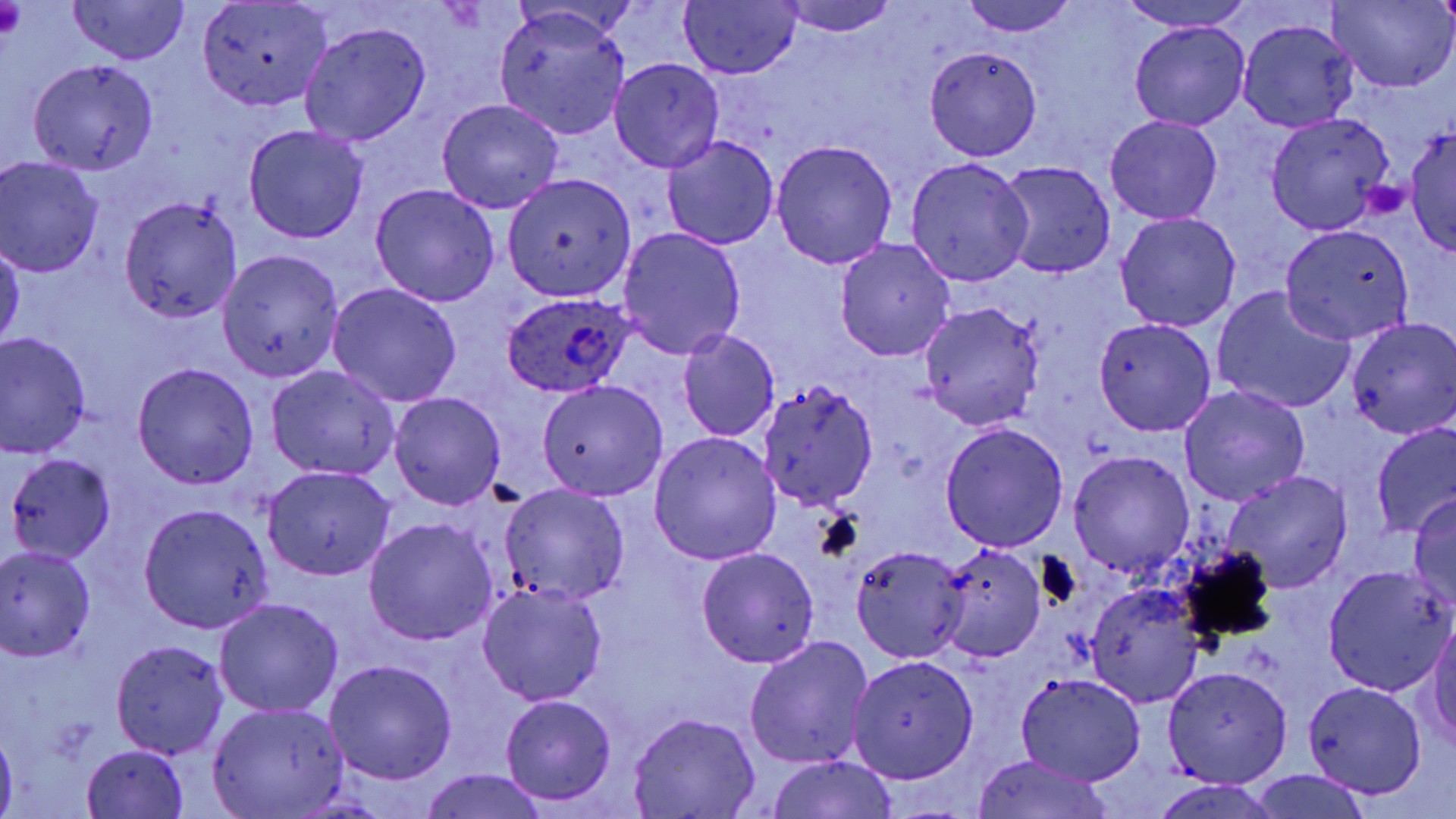

Summary:
  - Coordinate format: approximate bounding boxes as named x1/y1/x2/y2 corners in pixels
  - Platelet locations: (x1=0, y1=2, x2=28, y2=39), (x1=1361, y1=179, x2=1411, y2=220)
  - Uninfected red blood cell locations: (x1=67, y1=0, x2=189, y2=66), (x1=197, y1=0, x2=332, y2=112), (x1=956, y1=0, x2=1081, y2=36), (x1=1120, y1=0, x2=1253, y2=32), (x1=1330, y1=0, x2=1454, y2=91), (x1=681, y1=1, x2=802, y2=79), (x1=775, y1=1, x2=901, y2=36), (x1=493, y1=5, x2=632, y2=141), (x1=1131, y1=20, x2=1250, y2=130), (x1=1236, y1=20, x2=1358, y2=132), (x1=299, y1=22, x2=432, y2=146), (x1=923, y1=46, x2=1042, y2=160), (x1=609, y1=57, x2=725, y2=173), (x1=27, y1=58, x2=160, y2=175), (x1=436, y1=99, x2=565, y2=214), (x1=1265, y1=112, x2=1393, y2=235), (x1=1105, y1=114, x2=1223, y2=224), (x1=1404, y1=123, x2=1455, y2=256), (x1=243, y1=124, x2=369, y2=243), (x1=662, y1=135, x2=779, y2=251), (x1=769, y1=139, x2=896, y2=268), (x1=0, y1=157, x2=104, y2=277), (x1=905, y1=157, x2=1034, y2=285), (x1=993, y1=160, x2=1116, y2=281), (x1=503, y1=174, x2=635, y2=301), (x1=370, y1=183, x2=500, y2=307), (x1=119, y1=194, x2=243, y2=324), (x1=1115, y1=212, x2=1241, y2=332), (x1=1279, y1=223, x2=1417, y2=344), (x1=617, y1=227, x2=747, y2=361), (x1=835, y1=238, x2=956, y2=361), (x1=0, y1=241, x2=24, y2=355), (x1=219, y1=250, x2=344, y2=381), (x1=326, y1=282, x2=463, y2=407), (x1=1211, y1=288, x2=1354, y2=414), (x1=918, y1=302, x2=1044, y2=430), (x1=1095, y1=318, x2=1216, y2=435), (x1=1345, y1=318, x2=1456, y2=437), (x1=677, y1=328, x2=780, y2=442), (x1=1, y1=332, x2=95, y2=459), (x1=131, y1=363, x2=260, y2=489), (x1=265, y1=364, x2=401, y2=481), (x1=758, y1=379, x2=879, y2=512), (x1=536, y1=380, x2=669, y2=500), (x1=1176, y1=384, x2=1311, y2=507), (x1=388, y1=392, x2=506, y2=510), (x1=940, y1=422, x2=1070, y2=552), (x1=1371, y1=424, x2=1456, y2=537), (x1=649, y1=432, x2=782, y2=564), (x1=1068, y1=451, x2=1195, y2=579), (x1=5, y1=452, x2=116, y2=564), (x1=264, y1=465, x2=395, y2=580), (x1=1223, y1=469, x2=1352, y2=594), (x1=499, y1=482, x2=630, y2=606), (x1=1410, y1=492, x2=1456, y2=615), (x1=138, y1=502, x2=276, y2=633), (x1=364, y1=518, x2=497, y2=647), (x1=933, y1=543, x2=1046, y2=664), (x1=850, y1=544, x2=971, y2=663), (x1=0, y1=545, x2=98, y2=661), (x1=696, y1=547, x2=819, y2=668), (x1=1322, y1=565, x2=1453, y2=694), (x1=478, y1=581, x2=608, y2=706), (x1=1083, y1=581, x2=1207, y2=709), (x1=214, y1=598, x2=344, y2=719), (x1=1425, y1=613, x2=1456, y2=749), (x1=743, y1=637, x2=875, y2=771), (x1=111, y1=640, x2=229, y2=757), (x1=847, y1=656, x2=979, y2=783), (x1=323, y1=661, x2=457, y2=784), (x1=1162, y1=665, x2=1292, y2=787), (x1=1015, y1=672, x2=1148, y2=786), (x1=1301, y1=680, x2=1429, y2=799), (x1=500, y1=695, x2=617, y2=804), (x1=208, y1=702, x2=348, y2=817), (x1=627, y1=711, x2=762, y2=818), (x1=0, y1=727, x2=17, y2=819), (x1=81, y1=745, x2=190, y2=818), (x1=968, y1=753, x2=1116, y2=819), (x1=764, y1=756, x2=902, y2=819), (x1=420, y1=768, x2=547, y2=819), (x1=1250, y1=770, x2=1374, y2=819), (x1=1148, y1=779, x2=1285, y2=818)
  - Plasmodium ovale-infected red blood cell locations: (x1=502, y1=292, x2=632, y2=398)
  - Slide-level diagnosis: Plasmodium ovale
  - Preparation: thin blood smear
  - Field of view: one of a larger specimen
  - Stain: May-Grünwald-Giemsa
  - Image size: 1456×819 pixels
  - Modality: optical microscopy
  - Magnification: 1000x